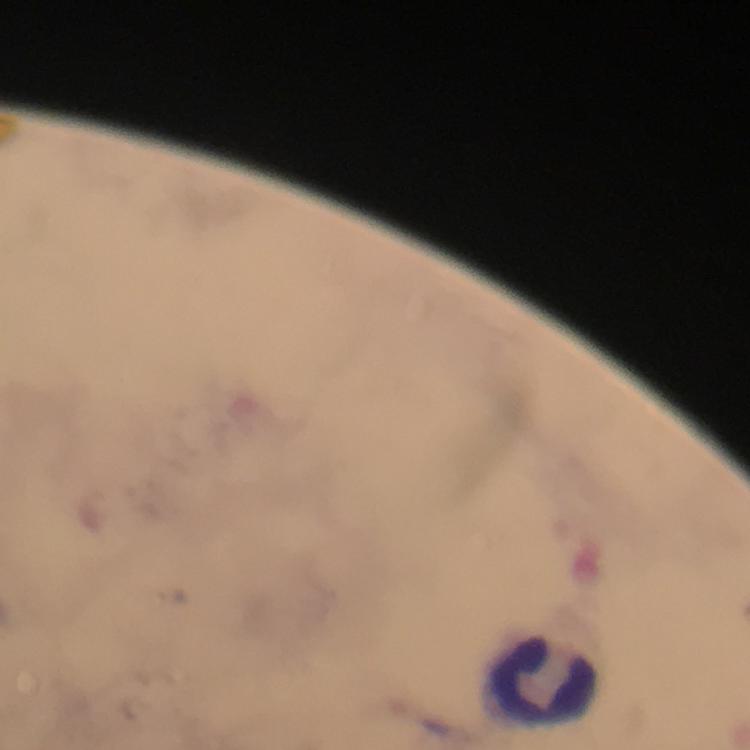
capture: smartphone mounted on the microscope
cropped_from: a single field of view
plasmodium_parasites: none seen
preparation: thick blood smear
image_size: 750×750 pixels
context: from a malaria diagnostic workup
magnification: 100x
stain: Giemsa
leukocyte_locations: 'approximate centers as [x, y] in pixels: [543, 685]'
immersion_oil: used